Give the extent of all Plasmodium vivax-infected red blood cells.
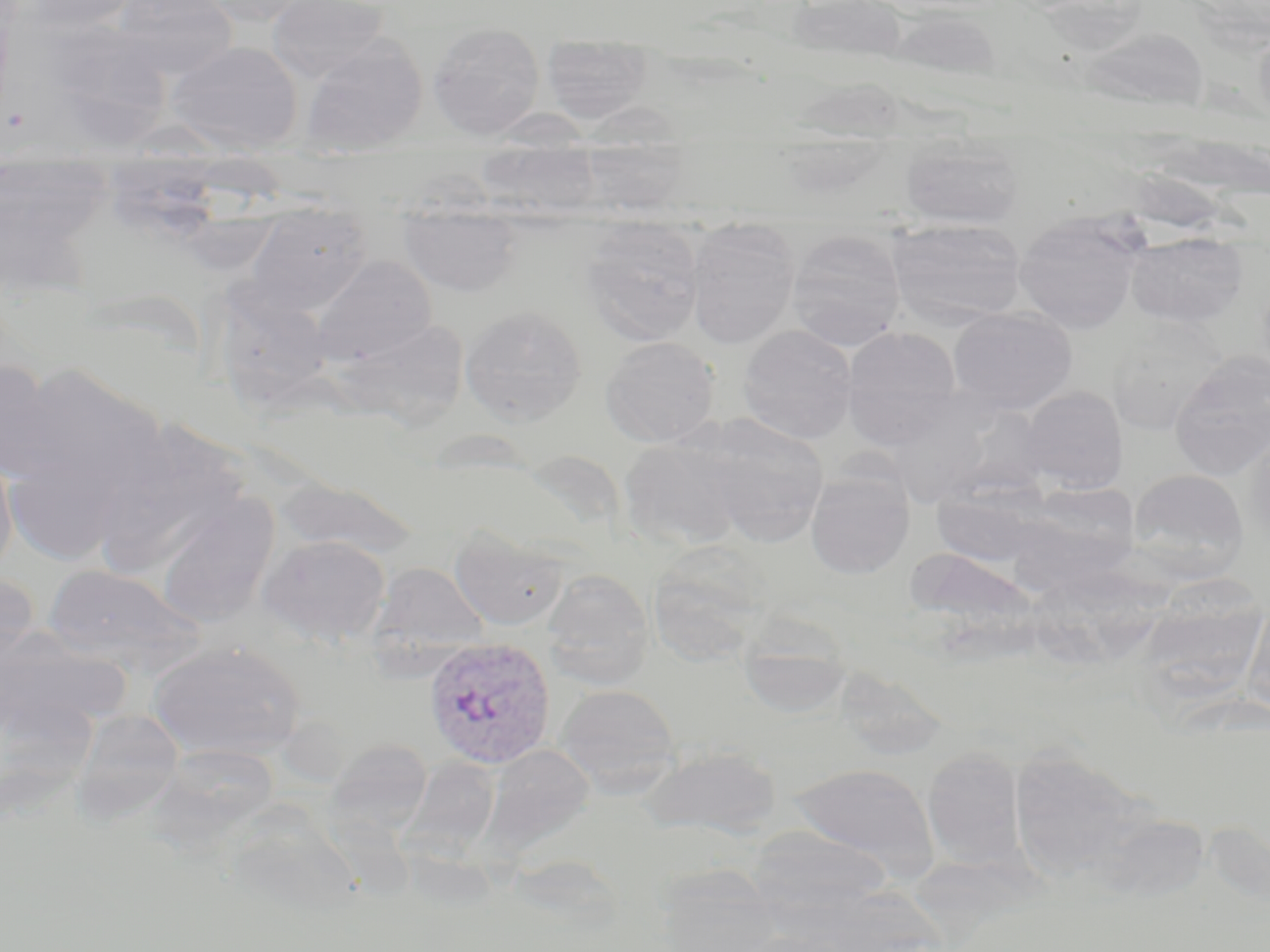
Approximate bounding boxes as named x1/y1/x2/y2 corners in pixels.
Plasmodium vivax-infected red blood cells: (x1=424, y1=637, x2=556, y2=769).

slide-level diagnosis = Plasmodium vivax
field of view = one of a larger specimen
preparation = thin blood film
stain = May-Grünwald-Giemsa
magnification = 1000x
modality = light microscopy
uninfected red blood cell locations = approximate bounding boxes as named x1/y1/x2/y2 corners in pixels: (x1=9, y1=0, x2=145, y2=35), (x1=111, y1=0, x2=238, y2=80), (x1=198, y1=0, x2=320, y2=26), (x1=266, y1=0, x2=390, y2=84), (x1=789, y1=1, x2=908, y2=69), (x1=34, y1=20, x2=174, y2=148), (x1=428, y1=21, x2=545, y2=140), (x1=1253, y1=22, x2=1270, y2=128), (x1=1075, y1=27, x2=1210, y2=113), (x1=540, y1=33, x2=654, y2=125), (x1=299, y1=34, x2=428, y2=154), (x1=166, y1=40, x2=303, y2=154), (x1=793, y1=76, x2=908, y2=142), (x1=590, y1=100, x2=695, y2=210), (x1=473, y1=110, x2=604, y2=203), (x1=114, y1=120, x2=242, y2=157), (x1=772, y1=136, x2=897, y2=201), (x1=899, y1=143, x2=1026, y2=230), (x1=185, y1=161, x2=289, y2=267), (x1=0, y1=164, x2=113, y2=283), (x1=241, y1=211, x2=376, y2=315), (x1=1014, y1=212, x2=1144, y2=334), (x1=399, y1=217, x2=525, y2=297), (x1=887, y1=219, x2=1027, y2=328), (x1=579, y1=223, x2=706, y2=345), (x1=685, y1=224, x2=801, y2=349), (x1=785, y1=228, x2=906, y2=350), (x1=1126, y1=233, x2=1247, y2=327), (x1=309, y1=256, x2=437, y2=368), (x1=205, y1=281, x2=337, y2=414), (x1=460, y1=305, x2=587, y2=425), (x1=947, y1=307, x2=1078, y2=415), (x1=1106, y1=318, x2=1229, y2=435), (x1=335, y1=319, x2=470, y2=428), (x1=738, y1=324, x2=857, y2=444), (x1=841, y1=326, x2=963, y2=449), (x1=600, y1=336, x2=720, y2=447), (x1=1169, y1=358, x2=1270, y2=481), (x1=0, y1=359, x2=72, y2=485), (x1=5, y1=360, x2=168, y2=552), (x1=1019, y1=386, x2=1129, y2=493), (x1=882, y1=395, x2=997, y2=508), (x1=931, y1=398, x2=1054, y2=501), (x1=687, y1=413, x2=830, y2=546), (x1=88, y1=420, x2=251, y2=575), (x1=1243, y1=427, x2=1270, y2=543), (x1=619, y1=437, x2=746, y2=551), (x1=0, y1=442, x2=18, y2=583), (x1=1128, y1=468, x2=1249, y2=579), (x1=805, y1=469, x2=914, y2=580), (x1=273, y1=478, x2=422, y2=559), (x1=929, y1=481, x2=1052, y2=567), (x1=1022, y1=482, x2=1142, y2=570), (x1=153, y1=496, x2=279, y2=627), (x1=448, y1=526, x2=570, y2=631), (x1=258, y1=534, x2=392, y2=647), (x1=646, y1=549, x2=771, y2=665), (x1=369, y1=561, x2=491, y2=659), (x1=43, y1=563, x2=206, y2=676), (x1=1028, y1=564, x2=1179, y2=663), (x1=541, y1=569, x2=654, y2=688), (x1=0, y1=574, x2=39, y2=678), (x1=1153, y1=576, x2=1265, y2=709), (x1=1241, y1=602, x2=1270, y2=719), (x1=735, y1=620, x2=854, y2=719), (x1=0, y1=629, x2=131, y2=735), (x1=147, y1=640, x2=306, y2=761), (x1=555, y1=683, x2=682, y2=796), (x1=69, y1=708, x2=184, y2=823), (x1=327, y1=738, x2=433, y2=835), (x1=485, y1=744, x2=595, y2=855), (x1=641, y1=745, x2=782, y2=838), (x1=923, y1=748, x2=1026, y2=871), (x1=1007, y1=749, x2=1150, y2=883), (x1=404, y1=755, x2=502, y2=855), (x1=790, y1=763, x2=941, y2=877), (x1=746, y1=825, x2=892, y2=921), (x1=653, y1=865, x2=784, y2=952)
image size = 1270×952 pixels